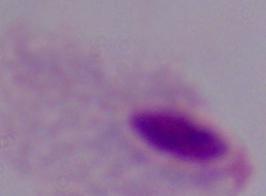

Summary:
  - Identification: trichomonad
  - Magnification: 1000x
  - Modality: micrograph